State which parasite is depicted.
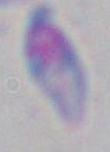

Toxoplasma gondii.

Captured at 1000x magnification. Photomicrograph.